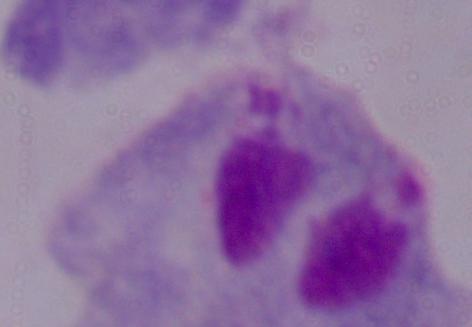
identification = trichomonad
modality = photomicrograph
magnification = 1000x